Locate every Plasmodium falciparum-infected red blood cell.
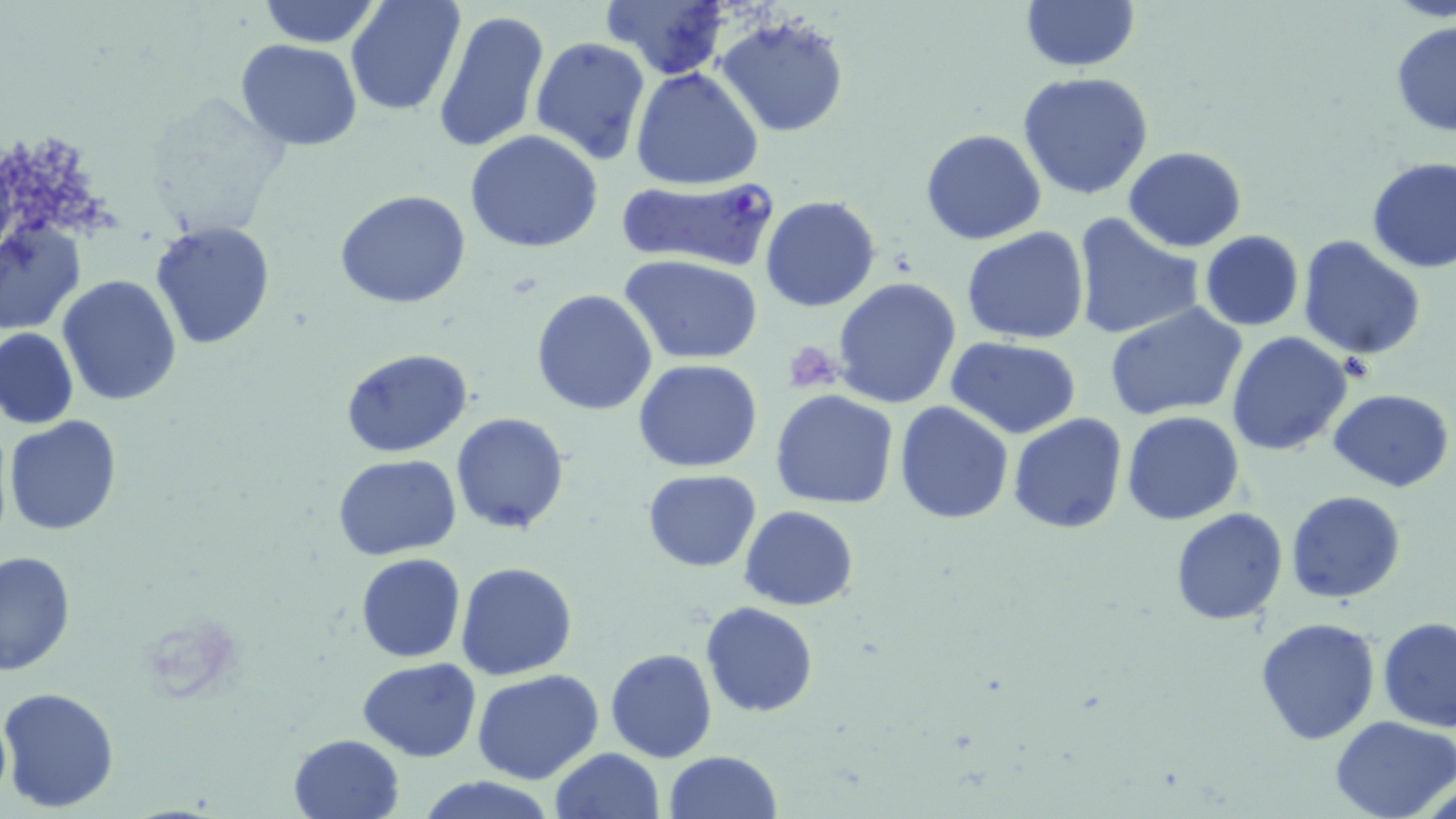
Approximate bounding boxes as (x1,y1)-(x2,y2) corner pairs in pixels.
Plasmodium falciparum-infected red blood cells: (614,177)-(778,268).

Summary:
  - Platelet locations: (785,341)-(844,395)
  - Uninfected red blood cell locations: (256,0)-(382,48), (344,0)-(467,117), (600,0)-(733,80), (1019,0)-(1140,73), (432,10)-(549,153), (715,13)-(849,137), (1391,19)-(1456,137), (531,37)-(651,167), (235,39)-(364,150), (632,68)-(765,190), (1017,71)-(1155,200), (141,93)-(290,239), (464,129)-(604,253), (920,130)-(1047,245), (1123,147)-(1248,252), (1366,157)-(1456,274), (335,191)-(472,309), (761,196)-(882,313), (1072,212)-(1203,342), (1,220)-(85,337), (149,223)-(276,350), (962,228)-(1090,346), (1199,230)-(1304,330), (1296,234)-(1427,360), (621,254)-(766,366), (57,275)-(183,407), (832,277)-(963,410), (532,289)-(657,414), (1105,304)-(1248,423), (0,327)-(79,430), (1226,331)-(1354,456), (946,336)-(1082,437), (340,347)-(474,457), (634,358)-(764,472), (1329,389)-(1454,492), (770,390)-(899,509), (896,402)-(1013,522), (451,411)-(570,534), (1122,412)-(1246,526), (1008,413)-(1128,534), (4,414)-(123,537), (332,454)-(461,560), (643,470)-(761,572), (1286,491)-(1405,604), (739,506)-(859,611), (1171,508)-(1288,625), (0,549)-(75,677), (356,553)-(465,663), (456,562)-(577,679), (701,602)-(817,717), (1256,616)-(1380,743), (1379,617)-(1456,733), (605,648)-(717,764), (358,658)-(483,761), (472,671)-(605,785), (1,685)-(119,812), (1330,714)-(1456,819), (289,733)-(403,818), (550,746)-(665,819), (664,750)-(783,819), (415,774)-(560,819)
  - Slide-level diagnosis: Plasmodium falciparum
  - Modality: light microscopy
  - Image size: 1456×819 pixels
  - Magnification: 1000x
  - Field of view: single
  - Preparation: thin blood film
  - Stain: May-Grünwald-Giemsa